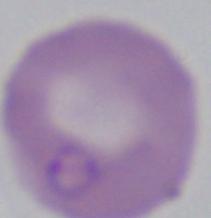
1000x magnification. A Babesia parasite is seen. Micrograph.